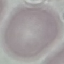

Summary:
  - Result: negative for malaria parasites
  - Image type: automatically extracted cell patch, resized to 64 × 64 pixels
  - Stain: Giemsa
  - Preparation: thin smear
  - Capture: smartphone through the microscope eyepiece